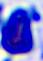
Summary:
  - Identification: white blood cell
  - Magnification: 400x
  - Modality: micrograph